Assess this cell for malaria.
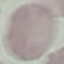
It is uninfected.

Cell patch, automatically extracted from a larger field of view and resized to 64 × 64 pixels. Acquired by smartphone through the microscope eyepiece. Thin blood smear. Giemsa stain.